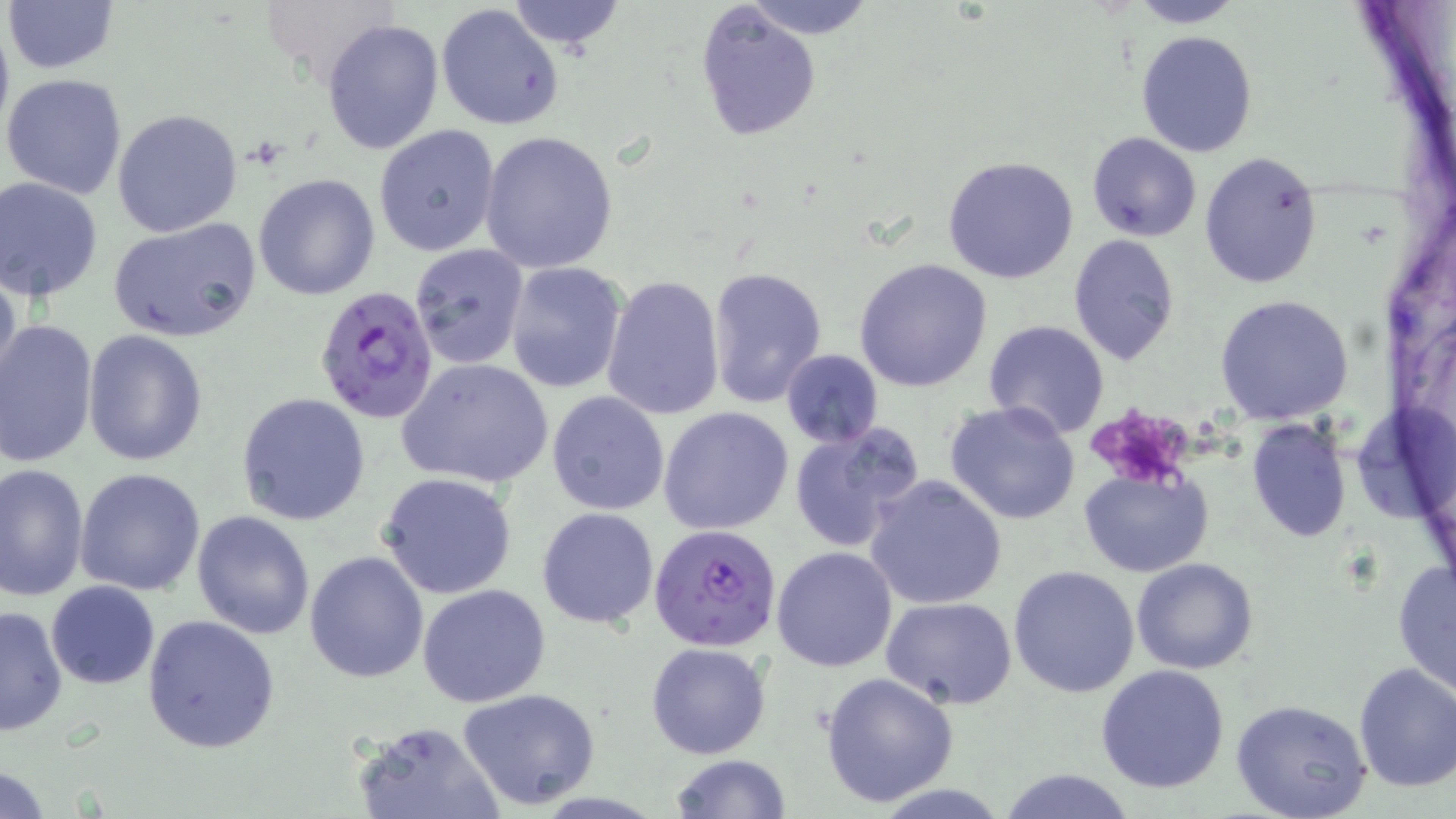

Summary:
  - Coordinate format: approximate bounding boxes as (x1, y1, x2, y2) in pixels
  - Platelet locations: (1095, 411, 1188, 489)
  - Plasmodium falciparum-infected red blood cell locations: (314, 284, 438, 424), (650, 522, 782, 651)
  - Uninfected red blood cell locations: (2, 0, 122, 76), (505, 0, 627, 55), (744, 0, 877, 37), (1122, 0, 1246, 28), (436, 4, 566, 132), (693, 4, 822, 142), (320, 18, 446, 157), (1135, 31, 1257, 158), (2, 72, 129, 198), (111, 108, 242, 237), (375, 123, 502, 257), (480, 130, 621, 273), (1085, 131, 1202, 241), (1199, 151, 1323, 289), (941, 155, 1080, 283), (252, 173, 380, 300), (0, 177, 105, 300), (108, 219, 262, 342), (1068, 234, 1180, 366), (409, 244, 528, 371), (854, 258, 992, 392), (504, 261, 629, 394), (0, 264, 23, 395), (705, 266, 828, 408), (602, 275, 725, 418), (1215, 295, 1355, 424), (1, 319, 99, 469), (983, 321, 1111, 440), (83, 330, 208, 467), (780, 348, 884, 449), (397, 357, 554, 488), (238, 392, 371, 525), (546, 392, 669, 516), (943, 401, 1081, 524), (659, 407, 794, 535), (1247, 418, 1350, 541), (788, 422, 924, 552), (0, 464, 89, 600), (74, 468, 206, 596), (1080, 469, 1213, 577), (377, 472, 518, 599), (863, 475, 1008, 609), (537, 507, 659, 628), (191, 511, 315, 639), (770, 545, 897, 670), (304, 550, 430, 684), (1131, 557, 1259, 675), (1392, 560, 1456, 696), (1009, 564, 1141, 699), (46, 581, 160, 688), (417, 583, 551, 707), (883, 596, 1018, 708), (0, 605, 69, 739), (142, 615, 281, 756), (646, 642, 770, 758), (1352, 662, 1456, 793), (1096, 665, 1231, 794), (820, 671, 959, 808), (458, 688, 601, 810), (1228, 698, 1373, 819), (350, 720, 505, 819), (668, 754, 793, 819), (0, 765, 55, 818), (997, 766, 1138, 819)
  - Slide-level diagnosis: Plasmodium falciparum
  - Modality: optical microscopy
  - Preparation: thin blood film
  - Image size: 1456×819 pixels
  - Stain: May-Grünwald-Giemsa
  - Magnification: 1000x
  - Field of view: single